Identify the blood parasite species.
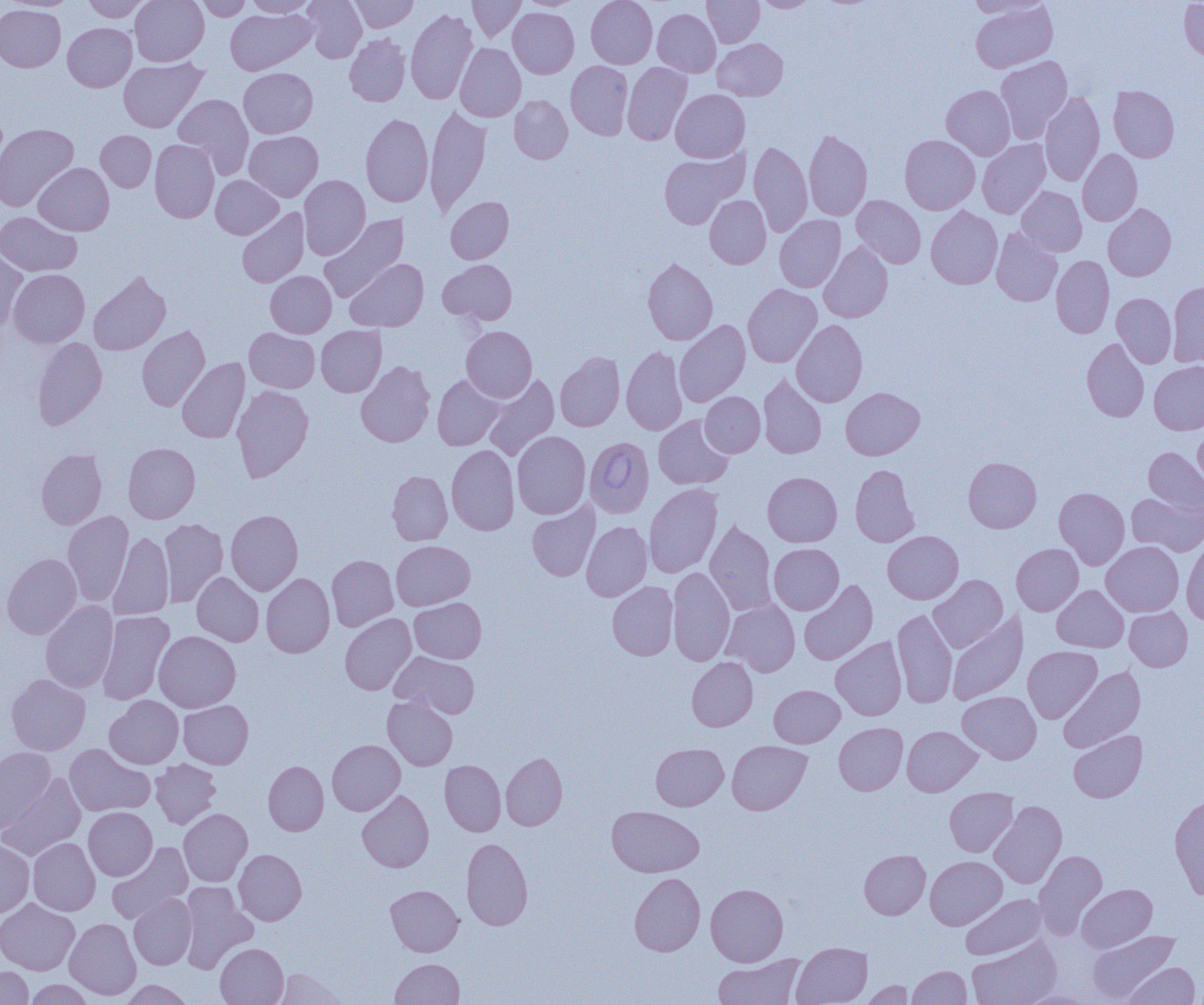
Babesia divergens.

{
  "image_size": "1204×1005 pixels",
  "modality": "optical microscopy",
  "preparation": "thin blood smear",
  "magnification": "1000x",
  "uninfected_red_blood_cell_locations": "approximate bounding boxes as named x1/y1/x2/y2 corners in pixels: (x1=3, y1=0, x2=80, y2=11), (x1=82, y1=0, x2=151, y2=22), (x1=130, y1=0, x2=209, y2=66), (x1=195, y1=0, x2=251, y2=21), (x1=246, y1=0, x2=315, y2=17), (x1=303, y1=0, x2=366, y2=63), (x1=350, y1=0, x2=419, y2=32), (x1=467, y1=0, x2=526, y2=42), (x1=517, y1=0, x2=582, y2=11), (x1=586, y1=0, x2=657, y2=68), (x1=702, y1=0, x2=764, y2=47), (x1=755, y1=0, x2=816, y2=12), (x1=965, y1=0, x2=1053, y2=18), (x1=1179, y1=1, x2=1204, y2=62), (x1=970, y1=2, x2=1058, y2=73), (x1=0, y1=5, x2=66, y2=72), (x1=225, y1=8, x2=316, y2=75), (x1=406, y1=8, x2=477, y2=105), (x1=508, y1=8, x2=579, y2=78), (x1=652, y1=8, x2=721, y2=77), (x1=63, y1=23, x2=136, y2=92), (x1=344, y1=33, x2=410, y2=106), (x1=712, y1=39, x2=788, y2=101), (x1=455, y1=43, x2=526, y2=122), (x1=995, y1=55, x2=1072, y2=143), (x1=119, y1=57, x2=208, y2=132), (x1=566, y1=61, x2=633, y2=139), (x1=622, y1=62, x2=692, y2=144), (x1=238, y1=68, x2=317, y2=138), (x1=941, y1=85, x2=1015, y2=160), (x1=1109, y1=86, x2=1179, y2=162), (x1=671, y1=89, x2=750, y2=162), (x1=1040, y1=92, x2=1105, y2=186), (x1=173, y1=94, x2=254, y2=177), (x1=510, y1=95, x2=572, y2=164), (x1=424, y1=105, x2=492, y2=215), (x1=361, y1=113, x2=433, y2=207), (x1=0, y1=123, x2=78, y2=212), (x1=804, y1=129, x2=872, y2=221), (x1=96, y1=130, x2=156, y2=192), (x1=244, y1=131, x2=323, y2=201), (x1=900, y1=135, x2=980, y2=214), (x1=150, y1=139, x2=219, y2=223), (x1=978, y1=139, x2=1051, y2=218), (x1=749, y1=141, x2=812, y2=237), (x1=658, y1=148, x2=749, y2=230), (x1=1078, y1=149, x2=1142, y2=225), (x1=33, y1=163, x2=114, y2=236), (x1=211, y1=175, x2=283, y2=239), (x1=299, y1=175, x2=370, y2=260), (x1=1016, y1=186, x2=1087, y2=256), (x1=704, y1=195, x2=771, y2=269), (x1=851, y1=195, x2=926, y2=268), (x1=445, y1=196, x2=513, y2=264), (x1=1103, y1=204, x2=1176, y2=281), (x1=926, y1=206, x2=1003, y2=289), (x1=237, y1=207, x2=310, y2=287), (x1=0, y1=212, x2=82, y2=277), (x1=319, y1=214, x2=408, y2=303), (x1=775, y1=215, x2=846, y2=292), (x1=991, y1=227, x2=1062, y2=306), (x1=818, y1=241, x2=893, y2=323), (x1=0, y1=246, x2=28, y2=333), (x1=1051, y1=255, x2=1114, y2=338), (x1=642, y1=258, x2=718, y2=345), (x1=345, y1=259, x2=428, y2=331), (x1=438, y1=260, x2=517, y2=324), (x1=7, y1=269, x2=89, y2=348), (x1=88, y1=271, x2=171, y2=355), (x1=266, y1=271, x2=336, y2=338), (x1=1167, y1=281, x2=1204, y2=367), (x1=743, y1=284, x2=822, y2=367), (x1=1111, y1=293, x2=1177, y2=368), (x1=674, y1=320, x2=750, y2=407), (x1=791, y1=320, x2=868, y2=407), (x1=316, y1=325, x2=387, y2=397), (x1=137, y1=326, x2=210, y2=411), (x1=461, y1=326, x2=537, y2=402), (x1=244, y1=328, x2=319, y2=393), (x1=32, y1=337, x2=107, y2=430), (x1=1082, y1=338, x2=1149, y2=421), (x1=621, y1=346, x2=687, y2=435), (x1=555, y1=352, x2=625, y2=431), (x1=177, y1=357, x2=250, y2=443), (x1=356, y1=361, x2=435, y2=447), (x1=1149, y1=361, x2=1204, y2=435), (x1=482, y1=373, x2=559, y2=461), (x1=758, y1=374, x2=826, y2=458), (x1=432, y1=375, x2=505, y2=451), (x1=232, y1=384, x2=313, y2=482), (x1=841, y1=387, x2=925, y2=460), (x1=701, y1=392, x2=765, y2=457), (x1=653, y1=415, x2=733, y2=489), (x1=1193, y1=426, x2=1204, y2=493), (x1=512, y1=430, x2=591, y2=519), (x1=123, y1=442, x2=200, y2=523), (x1=446, y1=445, x2=519, y2=535), (x1=1143, y1=447, x2=1204, y2=514), (x1=36, y1=449, x2=107, y2=529), (x1=963, y1=456, x2=1041, y2=533), (x1=850, y1=465, x2=919, y2=547), (x1=387, y1=470, x2=452, y2=545), (x1=763, y1=471, x2=842, y2=547), (x1=644, y1=483, x2=722, y2=578), (x1=1054, y1=487, x2=1129, y2=570), (x1=1126, y1=491, x2=1204, y2=555), (x1=527, y1=502, x2=600, y2=581), (x1=226, y1=509, x2=303, y2=595), (x1=62, y1=511, x2=133, y2=606), (x1=158, y1=518, x2=228, y2=607), (x1=705, y1=520, x2=777, y2=616), (x1=581, y1=521, x2=652, y2=601), (x1=883, y1=530, x2=963, y2=603), (x1=109, y1=531, x2=174, y2=621), (x1=1182, y1=538, x2=1204, y2=624), (x1=391, y1=540, x2=475, y2=610), (x1=1101, y1=541, x2=1184, y2=616), (x1=769, y1=543, x2=843, y2=614), (x1=1011, y1=544, x2=1083, y2=615), (x1=1, y1=553, x2=82, y2=640), (x1=327, y1=555, x2=398, y2=631), (x1=667, y1=567, x2=735, y2=667), (x1=192, y1=572, x2=264, y2=646), (x1=261, y1=573, x2=335, y2=658), (x1=928, y1=575, x2=1008, y2=653), (x1=607, y1=581, x2=678, y2=660), (x1=799, y1=581, x2=878, y2=665), (x1=1052, y1=585, x2=1128, y2=652), (x1=409, y1=598, x2=486, y2=663), (x1=720, y1=598, x2=800, y2=677), (x1=40, y1=600, x2=119, y2=693), (x1=1124, y1=606, x2=1192, y2=671), (x1=893, y1=608, x2=957, y2=708), (x1=96, y1=611, x2=174, y2=705), (x1=340, y1=613, x2=416, y2=695), (x1=947, y1=613, x2=1027, y2=705), (x1=153, y1=631, x2=240, y2=712), (x1=830, y1=636, x2=906, y2=720), (x1=1023, y1=646, x2=1102, y2=723), (x1=391, y1=651, x2=480, y2=718), (x1=687, y1=657, x2=758, y2=731), (x1=1058, y1=666, x2=1145, y2=752), (x1=6, y1=674, x2=90, y2=755), (x1=769, y1=685, x2=844, y2=748), (x1=957, y1=691, x2=1041, y2=764), (x1=105, y1=695, x2=184, y2=769), (x1=382, y1=695, x2=458, y2=770), (x1=178, y1=700, x2=253, y2=769), (x1=834, y1=722, x2=907, y2=795), (x1=902, y1=726, x2=981, y2=796), (x1=1068, y1=730, x2=1147, y2=802), (x1=327, y1=740, x2=405, y2=815), (x1=727, y1=741, x2=812, y2=815), (x1=64, y1=743, x2=154, y2=816), (x1=651, y1=743, x2=728, y2=810), (x1=0, y1=747, x2=56, y2=834), (x1=501, y1=752, x2=567, y2=830), (x1=150, y1=759, x2=221, y2=829), (x1=263, y1=760, x2=328, y2=835), (x1=440, y1=760, x2=506, y2=836), (x1=0, y1=772, x2=86, y2=861), (x1=945, y1=787, x2=1018, y2=856), (x1=357, y1=790, x2=434, y2=872), (x1=1169, y1=795, x2=1204, y2=899), (x1=990, y1=800, x2=1067, y2=888), (x1=607, y1=806, x2=704, y2=877), (x1=83, y1=807, x2=157, y2=880), (x1=178, y1=808, x2=253, y2=886), (x1=28, y1=838, x2=100, y2=916), (x1=461, y1=838, x2=533, y2=930), (x1=0, y1=840, x2=34, y2=917), (x1=107, y1=842, x2=193, y2=924), (x1=234, y1=849, x2=307, y2=925), (x1=859, y1=849, x2=930, y2=919), (x1=1033, y1=850, x2=1107, y2=937), (x1=925, y1=856, x2=1007, y2=929), (x1=629, y1=873, x2=705, y2=956), (x1=179, y1=883, x2=258, y2=974), (x1=705, y1=883, x2=788, y2=966), (x1=1077, y1=883, x2=1157, y2=952), (x1=385, y1=885, x2=463, y2=956), (x1=128, y1=894, x2=196, y2=970), (x1=960, y1=894, x2=1047, y2=960), (x1=0, y1=898, x2=80, y2=975), (x1=64, y1=917, x2=141, y2=1000), (x1=1087, y1=929, x2=1179, y2=1003), (x1=967, y1=937, x2=1062, y2=1005), (x1=791, y1=941, x2=872, y2=1005), (x1=215, y1=943, x2=289, y2=1005), (x1=712, y1=954, x2=806, y2=1005), (x1=390, y1=959, x2=464, y2=1004), (x1=1122, y1=961, x2=1200, y2=1005), (x1=907, y1=965, x2=971, y2=1005), (x1=0, y1=966, x2=32, y2=1004), (x1=271, y1=968, x2=346, y2=1004), (x1=25, y1=979, x2=94, y2=1004), (x1=121, y1=980, x2=194, y2=1005), (x1=860, y1=981, x2=915, y2=1004), (x1=1018, y1=990, x2=1093, y2=1004)",
  "field_of_view": "one of a larger specimen",
  "babesia_divergens_infected_red_blood_cell_locations": "approximate bounding boxes as named x1/y1/x2/y2 corners in pixels: (x1=585, y1=436, x2=654, y2=518)"
}